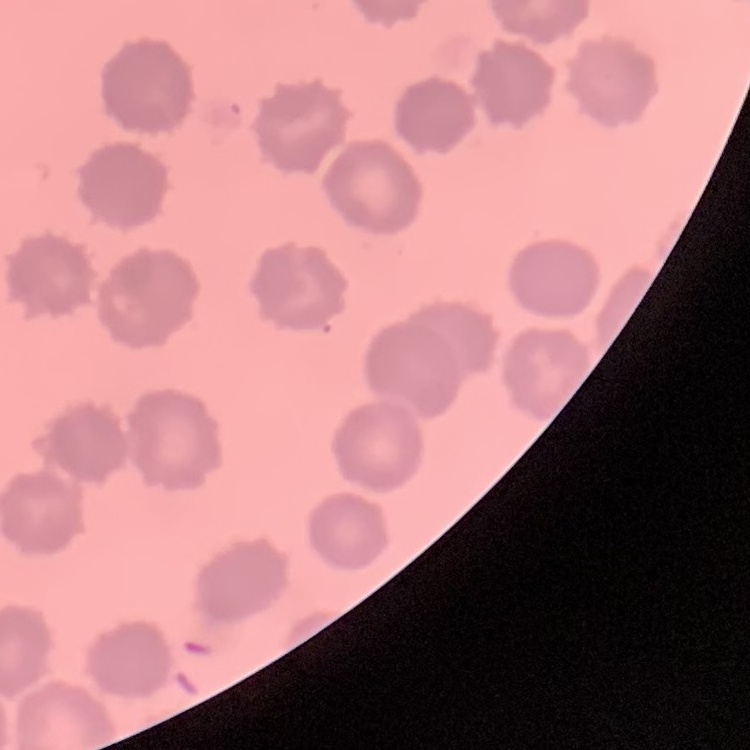

erythrocyte morphology = no rouleaux formation
stain = Field's or Giemsa
image type = square crop of a larger photomicrograph
preparation = thin blood smear